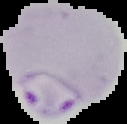

image type = segmented cell region with the area outside set to black
image size = 127×124 pixels
preparation = thin blood smear
malaria status = parasitized